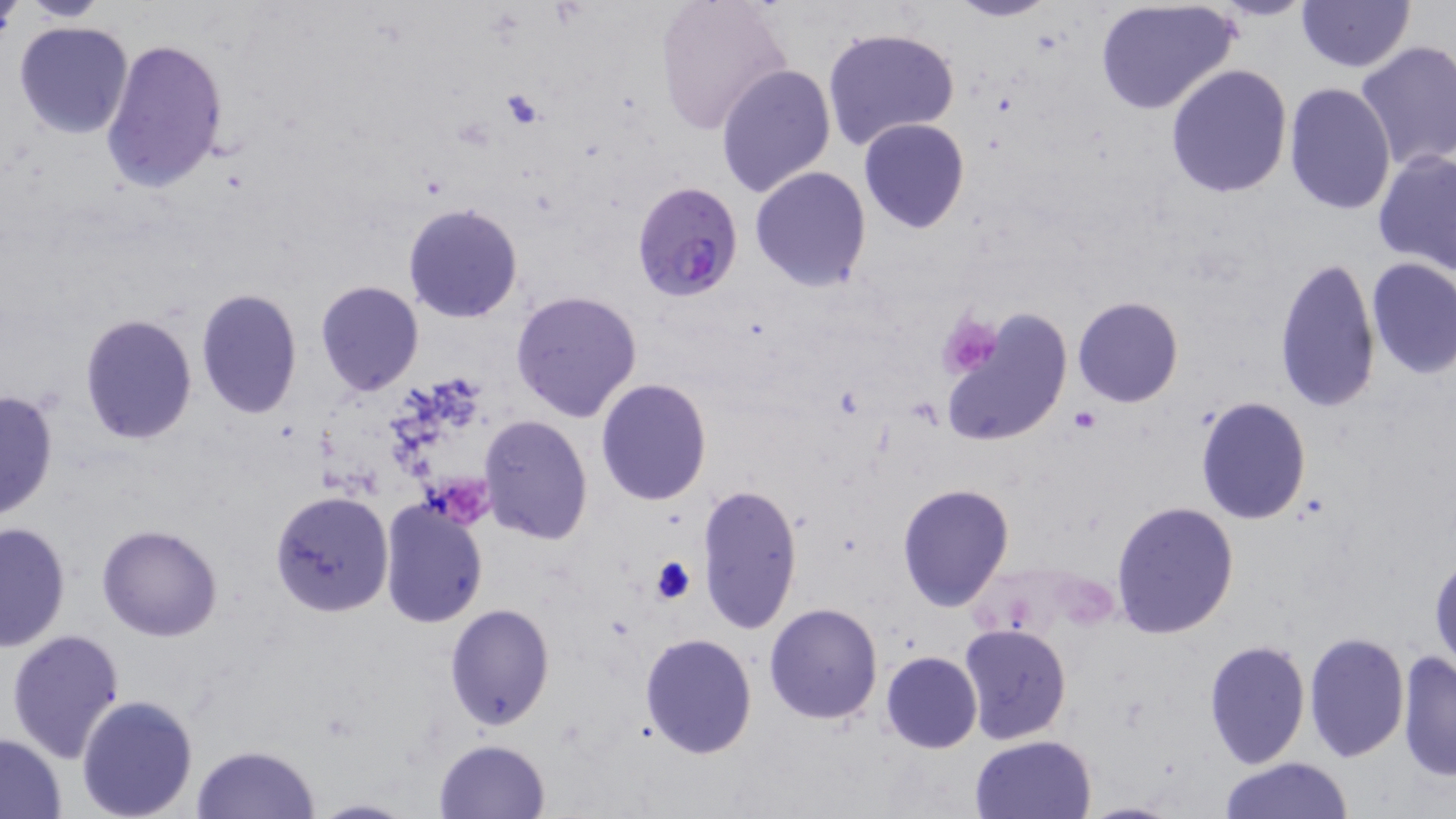

{
  "slide_level_diagnosis": "Plasmodium falciparum",
  "uninfected_red_blood_cell_locations": "approximate bounding boxes as (x1,y1)-(x2,y2) corner pairs in pixels: (0,0)-(23,44), (19,0)-(113,23), (653,0)-(792,135), (947,0)-(1059,22), (1093,0)-(1239,115), (1295,0)-(1415,72), (11,20)-(135,140), (823,26)-(961,155), (100,37)-(229,194), (1354,39)-(1456,172), (716,63)-(836,198), (1165,64)-(1293,197), (1282,83)-(1396,214), (858,118)-(969,233), (1373,147)-(1456,273), (749,166)-(873,292), (404,203)-(523,324), (1273,255)-(1380,414), (1365,257)-(1456,380), (315,281)-(424,397), (196,287)-(301,417), (510,290)-(643,424), (1073,296)-(1183,407), (941,311)-(1073,447), (78,313)-(198,444), (594,378)-(711,506), (0,389)-(60,524), (1195,397)-(1312,524), (480,415)-(592,544), (895,482)-(1014,611), (696,483)-(804,635), (270,490)-(393,617), (378,498)-(487,628), (1110,500)-(1240,639), (0,521)-(71,652), (97,524)-(222,641), (1429,551)-(1455,676), (763,602)-(883,724), (444,603)-(555,732), (957,624)-(1072,746), (6,629)-(126,763), (1304,631)-(1409,761), (640,632)-(758,758), (1204,639)-(1310,768), (1396,649)-(1456,783), (881,650)-(982,753), (77,695)-(199,819), (0,734)-(68,816), (970,735)-(1096,819), (433,739)-(551,819), (191,745)-(320,819), (1217,757)-(1356,817), (305,796)-(415,818)",
  "stain": "May-Grünwald-Giemsa",
  "modality": "light microscopy",
  "magnification": "1000x",
  "image_size": "1456×819 pixels",
  "field_of_view": "single",
  "plasmodium_falciparum_infected_red_blood_cell_locations": "approximate bounding boxes as (x1,y1)-(x2,y2) corner pairs in pixels: (629,180)-(744,301)",
  "platelet_locations": "approximate bounding boxes as (x1,y1)-(x2,y2) corner pairs in pixels: (498,88)-(549,130), (936,312)-(1006,379), (1071,408)-(1102,433), (649,554)-(697,605)",
  "preparation": "thin blood smear"
}